Identify the parasite.
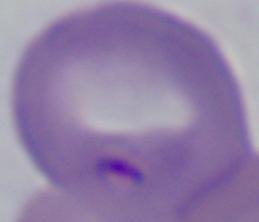

This is Babesia.

Summary:
  - Magnification: 1000x
  - Modality: photomicrograph